Classify this cell by malaria status.
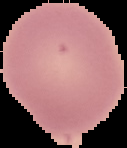
It is uninfected.

image size = 127×148 pixels
image type = segmented cell region with the area outside set to black
preparation = thin blood film